Give the position of every Plasmodium parasite.
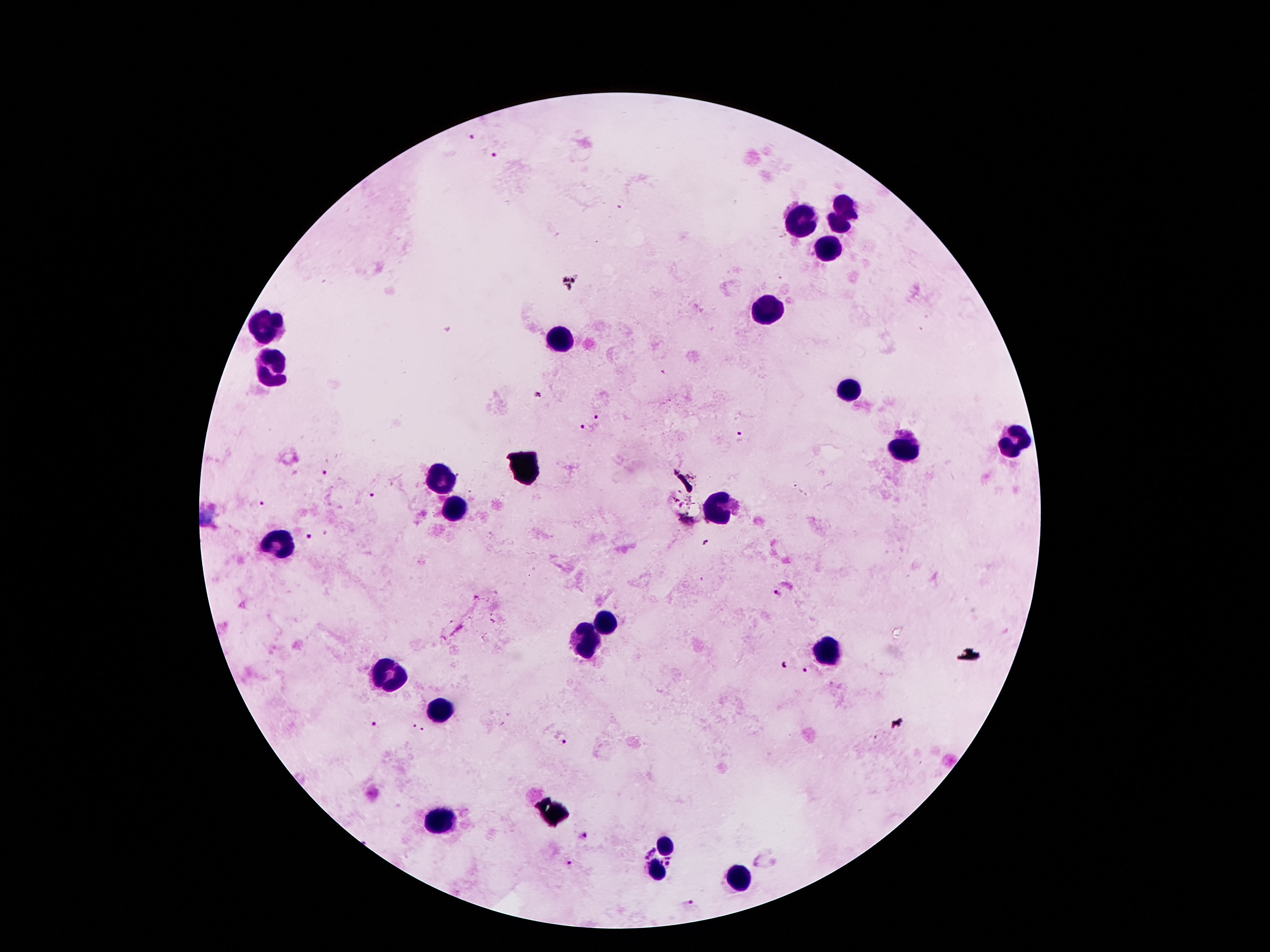

Approximate centers as (x, y) in pixels.
Plasmodium parasites: (470, 135), (497, 155), (599, 418), (585, 429), (740, 437), (326, 474), (371, 494), (261, 504), (310, 536), (776, 593), (783, 666), (804, 670), (377, 725), (415, 726), (425, 730), (563, 741), (583, 838), (649, 852), (569, 864), (689, 904).

Summary:
  - Leukocyte locations: (845, 202), (805, 220), (838, 224), (827, 251), (764, 308), (271, 320), (561, 341), (273, 369), (852, 390), (1011, 436), (906, 450), (437, 477), (452, 506), (721, 509), (278, 542), (607, 623), (595, 640), (830, 653), (385, 676), (438, 712), (439, 823), (663, 847), (655, 873), (735, 878)
  - Image size: 1270×952 pixels
  - Preparation: thick peripheral-blood smear
  - Stain: Giemsa
  - Patient malaria status: infected with Plasmodium falciparum
  - Magnification: 100x
  - Field of view: single
  - Capture: smartphone through the microscope eyepiece